Identify the parasite.
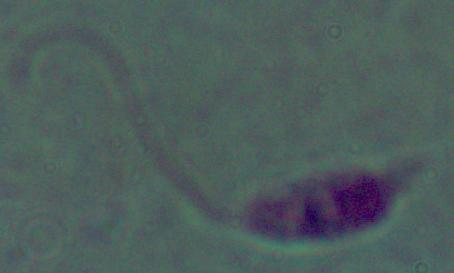

This is Leishmania.

Summary:
  - Modality: micrograph
  - Magnification: 1000x